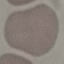
Summary:
  - Result: negative for malaria parasites
  - Image type: automatically extracted cell patch, resized to 64 × 64 pixels
  - Preparation: thin blood smear
  - Stain: Giemsa
  - Capture: smartphone camera at the microscope eyepiece